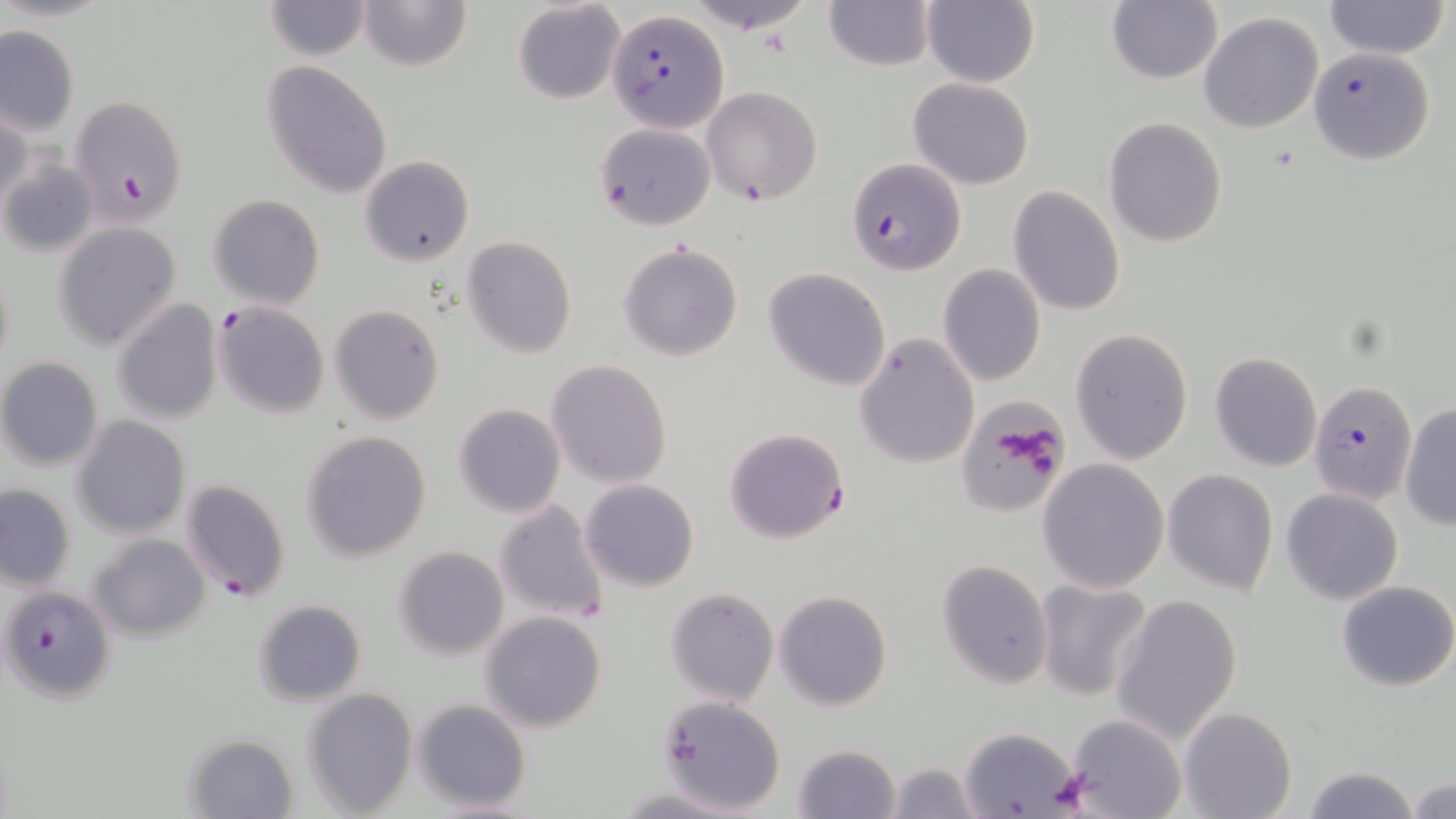

Approximate bounding boxes as (x1, y1, x2, y2) in pixels. Plasmodium falciparum-infected red blood cell locations: (607, 8, 727, 131), (1308, 46, 1436, 166), (0, 156, 96, 257), (847, 157, 964, 277), (214, 301, 330, 418), (1309, 381, 1418, 504), (723, 426, 850, 544), (181, 478, 291, 603), (2, 585, 116, 706). Uninfected red blood cell locations: (262, 0, 374, 61), (356, 0, 472, 72), (921, 0, 1038, 88), (682, 1, 820, 33), (825, 1, 935, 72), (1107, 1, 1221, 84), (1323, 1, 1450, 59), (513, 2, 626, 104), (1198, 12, 1325, 134), (0, 23, 79, 137), (260, 62, 394, 199), (907, 77, 1035, 189), (701, 85, 822, 206), (69, 93, 188, 227), (0, 98, 29, 215), (1103, 116, 1228, 248), (593, 123, 716, 231), (360, 155, 474, 266), (1008, 185, 1126, 316), (208, 193, 325, 309), (52, 222, 182, 351), (460, 236, 578, 358), (618, 242, 745, 362), (938, 263, 1046, 387), (763, 268, 892, 392), (111, 299, 224, 424), (328, 304, 446, 426), (1070, 328, 1194, 466), (853, 331, 981, 469), (1209, 351, 1324, 473), (0, 357, 105, 470), (546, 360, 673, 487), (1399, 401, 1455, 529), (451, 402, 566, 518), (71, 416, 192, 539), (300, 430, 433, 561), (1037, 459, 1169, 593), (1162, 469, 1281, 595), (579, 478, 700, 593), (1, 483, 76, 590), (1281, 487, 1403, 605), (492, 500, 611, 625), (87, 534, 211, 642), (392, 545, 509, 661), (937, 561, 1053, 688), (1033, 577, 1155, 702), (1336, 580, 1456, 693), (665, 587, 780, 707), (773, 590, 893, 711), (1110, 594, 1243, 745), (250, 599, 368, 708), (479, 611, 608, 733), (300, 687, 418, 816), (652, 695, 786, 814), (410, 699, 533, 813), (1178, 707, 1297, 819), (1061, 713, 1189, 819), (958, 726, 1081, 818), (181, 731, 299, 817), (792, 742, 901, 819), (883, 761, 981, 819), (1300, 765, 1421, 819), (1407, 777, 1455, 818), (609, 787, 753, 817). Platelet locations: (965, 405, 1064, 505). Slide-level diagnosis: Plasmodium falciparum. One field of a larger specimen. Thin blood film. 1000x magnification. May-Grünwald-Giemsa stain. Image is 1456×819 pixels. Light microscopy.